Locate and identify every blood parasite.
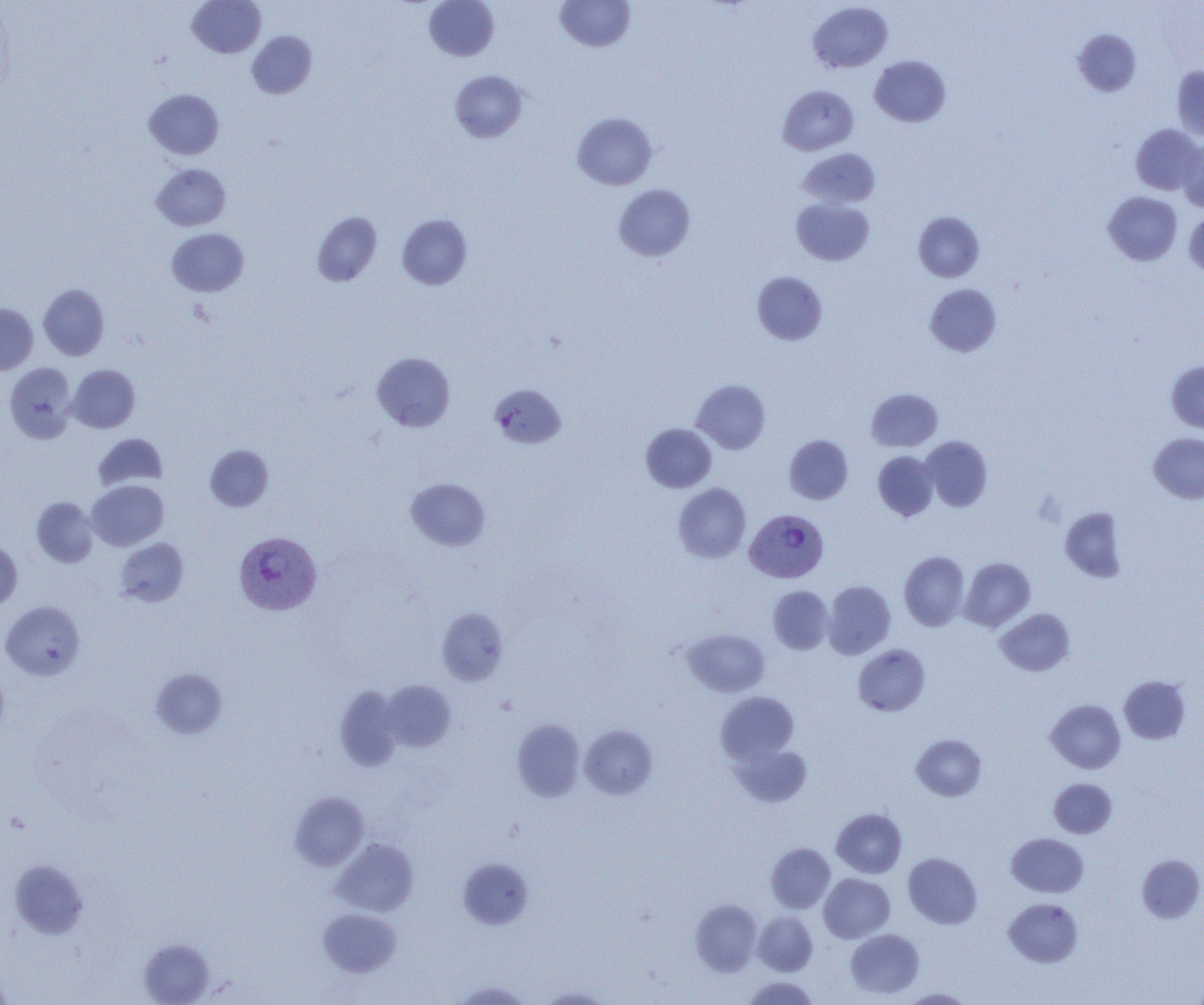
Approximate bounding boxes as [x1, y1, x2, y2] in pixels.
Plasmodium vivax-infected red blood cells: [745, 508, 829, 583], [233, 531, 322, 616].
No Plasmodium falciparum, Plasmodium ovale, Plasmodium malariae, Babesia divergens, or Trypanosoma brucei observed.

Uninfected red blood cell locations: [187, 0, 266, 58], [423, 0, 500, 61], [555, 1, 635, 52], [808, 2, 893, 73], [1073, 29, 1141, 96], [247, 31, 317, 99], [869, 55, 951, 127], [1171, 66, 1204, 141], [450, 70, 528, 143], [777, 85, 858, 155], [143, 89, 224, 160], [572, 112, 657, 190], [1130, 124, 1202, 195], [1177, 140, 1204, 212], [798, 148, 880, 208], [151, 163, 231, 230], [614, 184, 695, 261], [1103, 191, 1183, 265], [792, 198, 874, 265], [1184, 210, 1204, 278], [312, 212, 382, 286], [913, 212, 985, 282], [397, 213, 473, 290], [166, 228, 249, 296], [752, 271, 827, 345], [925, 283, 1001, 356], [38, 284, 109, 360], [0, 303, 38, 375], [372, 352, 455, 432], [1167, 361, 1204, 433], [4, 362, 77, 443], [67, 365, 140, 432], [691, 379, 771, 453], [490, 384, 566, 448], [866, 388, 942, 451], [641, 423, 716, 492], [93, 433, 168, 491], [1148, 433, 1204, 503], [784, 435, 853, 504], [921, 436, 993, 511], [205, 445, 274, 511], [873, 451, 939, 521], [406, 478, 490, 550], [86, 480, 168, 550], [673, 483, 751, 562], [32, 497, 99, 568], [1059, 506, 1127, 582], [115, 537, 188, 606], [0, 539, 22, 610], [899, 551, 969, 630], [959, 557, 1035, 631], [822, 580, 896, 659], [768, 585, 834, 654], [1, 601, 85, 680], [437, 608, 508, 686], [995, 608, 1076, 676], [683, 629, 769, 697], [853, 644, 930, 716], [0, 665, 9, 741], [151, 668, 228, 738], [1119, 675, 1190, 744], [381, 680, 456, 751], [335, 686, 402, 771], [716, 692, 799, 765], [1046, 699, 1125, 773], [512, 719, 586, 801], [580, 725, 657, 799], [911, 734, 987, 801], [729, 742, 812, 808], [1049, 778, 1117, 838], [290, 792, 369, 870], [832, 808, 907, 877], [1006, 833, 1089, 897], [332, 838, 418, 916], [766, 843, 835, 913], [903, 852, 982, 928], [1137, 854, 1204, 923], [458, 858, 534, 929], [10, 859, 88, 939], [818, 873, 895, 943], [1004, 898, 1083, 967], [690, 899, 763, 975], [318, 908, 401, 977], [753, 912, 818, 975], [846, 928, 924, 998], [139, 938, 215, 1005], [0, 972, 13, 1004], [741, 976, 820, 1004], [452, 981, 533, 1004], [539, 986, 613, 1004], [900, 988, 973, 1004]. Slide-level diagnosis: Plasmodium vivax. Image is 1204×1005 pixels. Thin blood smear. Single field of view. Optical microscopy. 1000x magnification.